Name the parasite shown.
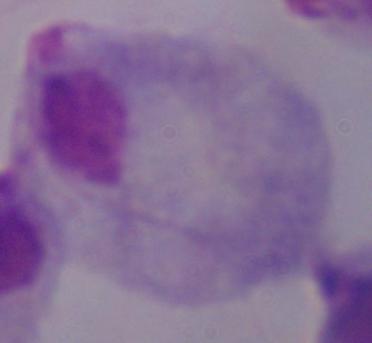
This is a trichomonad.

Summary:
  - Modality: micrograph
  - Magnification: 1000x